State which cell type is depicted.
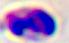

A leukocyte.

modality = photomicrograph
magnification = 400x